Report the malaria status of this cell.
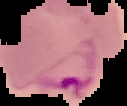

Parasitized.

image size = 127×106 pixels
image type = segmented cell region on a black background
preparation = thin blood film